Outline each Babesia divergens-infected red blood cell.
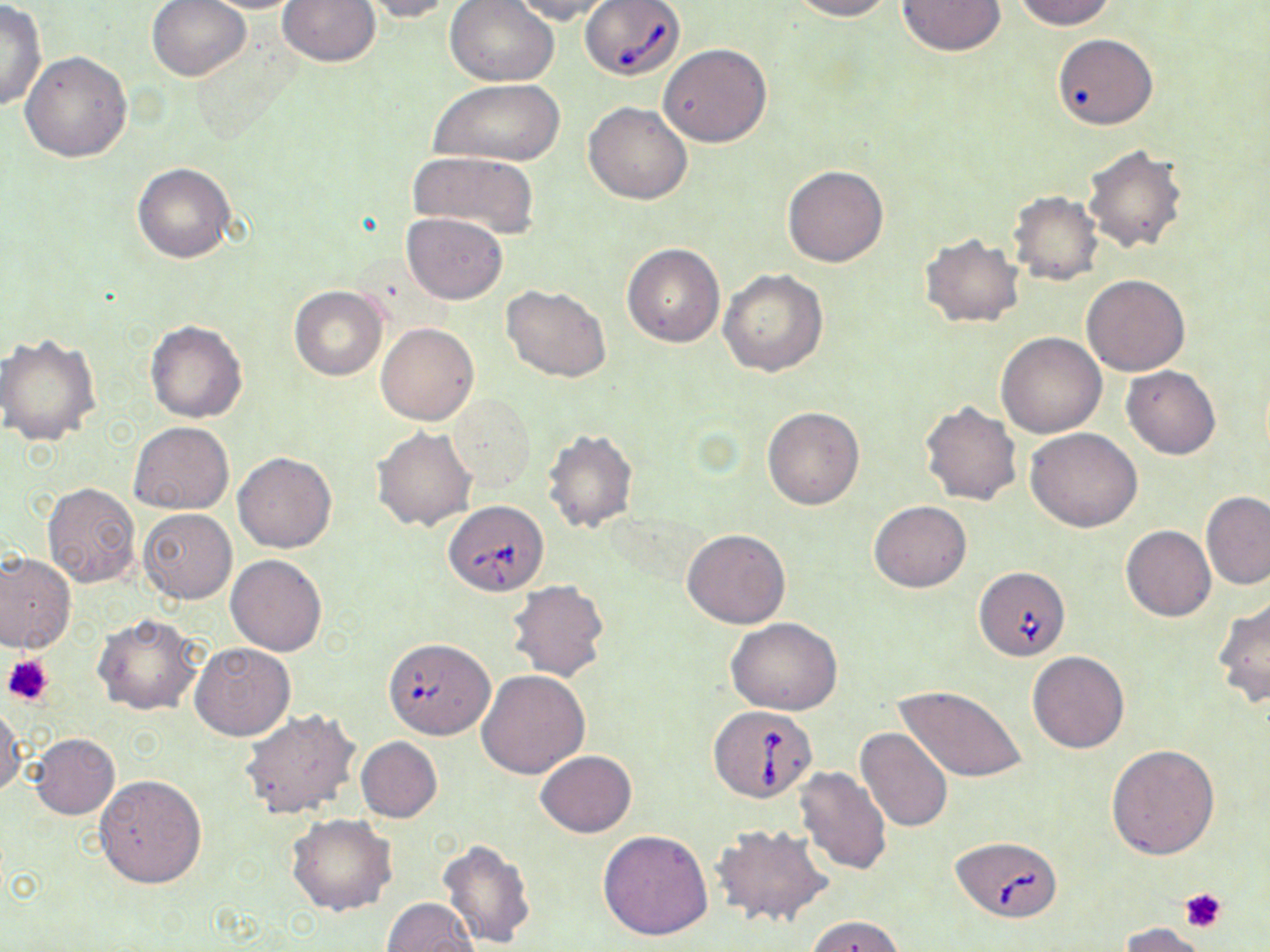

Approximate bounding boxes as (x1, y1, x2, y2) in pixels.
Babesia divergens-infected red blood cells: (579, 1, 685, 81), (444, 500, 547, 595), (973, 565, 1069, 661), (710, 705, 817, 802), (950, 835, 1062, 921).

Summary:
  - Platelet locations: (3, 652, 56, 707), (1179, 888, 1227, 932)
  - Uninfected red blood cell locations: (147, 0, 251, 82), (191, 0, 309, 13), (278, 0, 380, 67), (354, 0, 458, 22), (508, 0, 621, 24), (786, 0, 895, 21), (1014, 0, 1117, 30), (445, 1, 559, 84), (896, 1, 1005, 55), (0, 2, 47, 113), (1051, 34, 1155, 130), (658, 43, 772, 146), (20, 51, 131, 162), (431, 79, 564, 166), (585, 101, 692, 204), (1082, 144, 1190, 255), (407, 151, 542, 238), (132, 162, 235, 263), (781, 165, 888, 268), (1008, 191, 1102, 284), (401, 212, 507, 303), (921, 233, 1024, 328), (622, 242, 725, 348), (718, 268, 828, 377), (1082, 274, 1190, 376), (502, 284, 611, 383), (288, 285, 388, 381), (145, 320, 247, 423), (375, 323, 479, 425), (997, 332, 1108, 438), (1, 333, 103, 447), (1121, 365, 1221, 459), (449, 395, 535, 490), (919, 400, 1023, 506), (763, 406, 864, 509), (129, 422, 234, 515), (1027, 426, 1143, 532), (372, 427, 478, 531), (542, 428, 640, 533), (234, 453, 336, 553), (42, 482, 141, 587), (1202, 492, 1270, 591), (868, 500, 972, 592), (137, 510, 236, 602), (1121, 525, 1216, 622), (682, 528, 790, 629), (0, 551, 75, 654), (226, 554, 327, 657), (506, 579, 609, 683), (1213, 597, 1270, 709), (92, 613, 203, 715), (726, 617, 842, 715), (383, 637, 495, 739), (189, 641, 296, 742), (1027, 650, 1130, 753), (476, 670, 590, 779), (896, 684, 1026, 784), (0, 702, 23, 798), (239, 709, 361, 820), (855, 727, 954, 833), (29, 733, 120, 820), (356, 737, 442, 822), (1107, 744, 1220, 859), (536, 750, 637, 836), (793, 768, 892, 875), (94, 775, 207, 889), (286, 814, 398, 916), (710, 824, 833, 929), (597, 828, 714, 939), (438, 838, 536, 948), (382, 898, 480, 952), (805, 915, 906, 952), (1117, 922, 1211, 951)
  - Slide-level diagnosis: Babesia divergens
  - Magnification: 1000x
  - Field of view: one of a larger specimen
  - Preparation: thin blood film
  - Modality: light microscopy
  - Image size: 1270×952 pixels
  - Stain: May-Grünwald-Giemsa